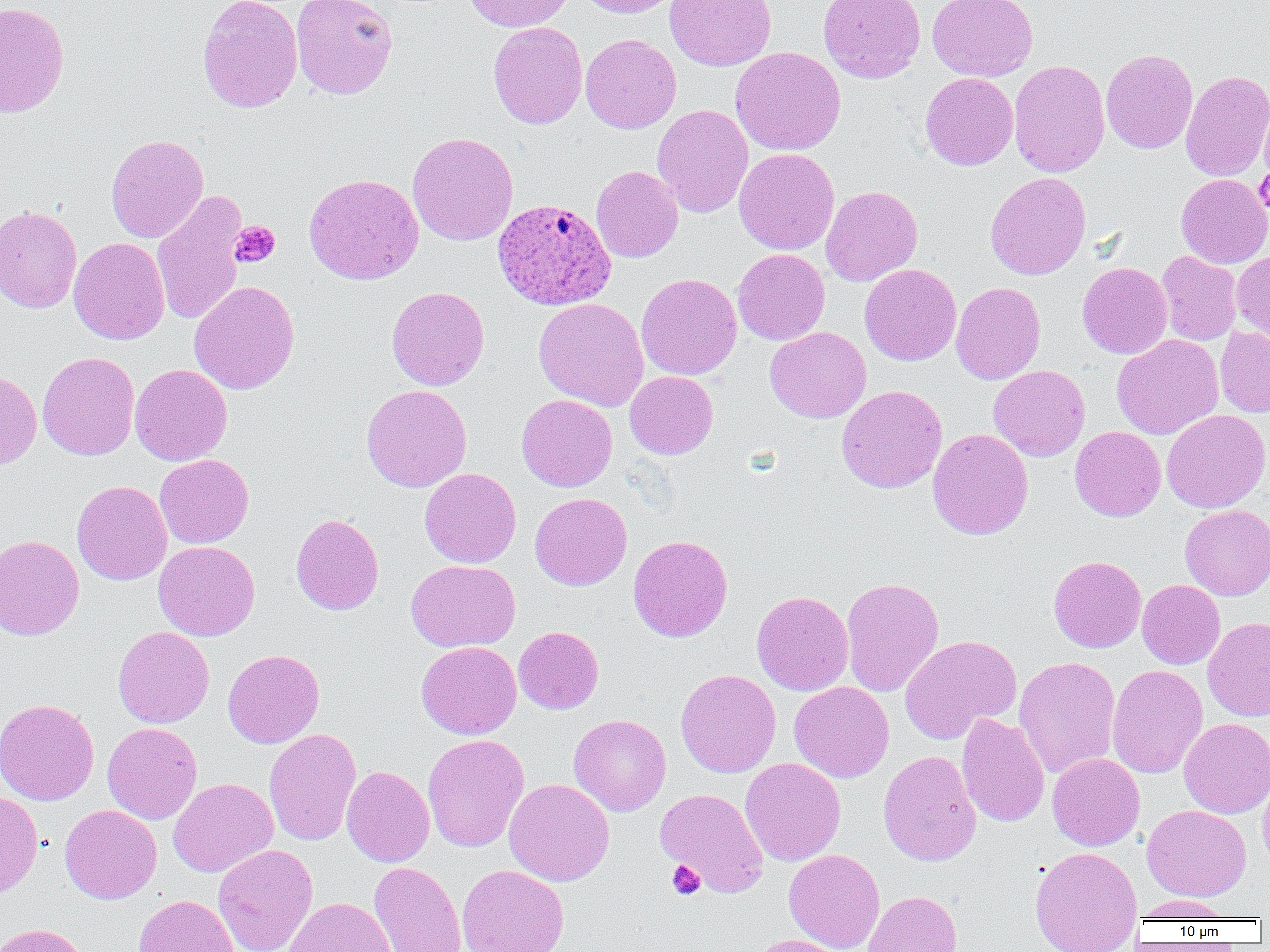

slide-level diagnosis = Plasmodium ovale
field of view = single
magnification = 1000x
Plasmodium ovale-infected red blood cell locations = approximate bounding boxes as [x1, y1, x2, y2] in pixels: [492, 198, 617, 311]
modality = optical microscopy
image size = 1270×952 pixels
preparation = thin blood film
uninfected red blood cell locations = approximate bounding boxes as [x1, y1, x2, y2] in pixels: [291, 0, 398, 99], [463, 0, 573, 32], [575, 0, 683, 18], [664, 0, 777, 71], [818, 0, 926, 84], [927, 0, 1038, 82], [197, 1, 302, 113], [0, 2, 69, 118], [488, 22, 587, 130], [580, 33, 681, 134], [730, 46, 846, 155], [1101, 48, 1198, 154], [1009, 59, 1110, 177], [1180, 70, 1270, 181], [920, 72, 1018, 170], [1258, 90, 1270, 186], [652, 104, 753, 217], [407, 132, 519, 246], [106, 134, 209, 243], [734, 148, 839, 255], [591, 165, 684, 263], [985, 172, 1092, 280], [303, 173, 424, 284], [1176, 174, 1270, 268], [821, 185, 922, 286], [151, 190, 248, 326], [0, 205, 82, 313], [69, 237, 169, 345], [733, 249, 830, 345], [1232, 250, 1270, 346], [1156, 251, 1242, 345], [1077, 262, 1172, 359], [860, 264, 961, 366], [636, 273, 742, 380], [189, 280, 300, 394], [951, 282, 1046, 385], [386, 286, 489, 391], [533, 298, 649, 410], [765, 326, 871, 423], [1215, 327, 1270, 417], [1111, 334, 1224, 440], [37, 352, 140, 460], [130, 364, 232, 466], [989, 365, 1090, 461], [0, 370, 42, 469], [624, 371, 718, 459], [361, 384, 472, 492], [836, 385, 947, 494], [517, 394, 617, 492], [1161, 409, 1270, 513], [1070, 426, 1166, 521], [927, 428, 1034, 540], [154, 454, 253, 548], [419, 468, 521, 568], [72, 480, 172, 585], [529, 492, 632, 590], [1180, 505, 1270, 601], [290, 513, 384, 615], [628, 534, 733, 642], [0, 535, 85, 640], [153, 541, 259, 641], [1048, 555, 1146, 652], [405, 559, 520, 651], [841, 577, 944, 697], [1137, 579, 1225, 669], [751, 591, 854, 695], [1203, 617, 1270, 721], [113, 626, 214, 728], [514, 626, 603, 714], [900, 635, 1021, 744], [416, 641, 521, 739], [222, 649, 324, 748], [1014, 656, 1120, 779], [1106, 664, 1207, 778], [676, 669, 781, 777], [789, 681, 894, 783], [0, 698, 99, 806], [957, 713, 1050, 828], [568, 714, 671, 816], [1179, 718, 1270, 818], [102, 722, 203, 824], [264, 728, 361, 846], [422, 734, 529, 853], [878, 750, 981, 866], [1047, 752, 1145, 851], [740, 757, 846, 866], [341, 766, 434, 867], [1258, 768, 1270, 875], [168, 778, 278, 877], [504, 779, 614, 886], [654, 788, 769, 898], [0, 791, 44, 898], [60, 804, 162, 904], [1142, 804, 1251, 901], [213, 845, 318, 952], [1029, 846, 1143, 952], [784, 849, 885, 952], [368, 861, 466, 952], [458, 864, 570, 952], [863, 891, 962, 952], [133, 895, 238, 952], [1135, 895, 1233, 921], [284, 897, 396, 952], [0, 923, 90, 952], [746, 934, 848, 952]
platelet locations = approximate bounding boxes as [x1, y1, x2, y2] in pixels: [1254, 167, 1270, 215], [229, 221, 280, 268], [666, 860, 705, 901]